Outline each Plasmodium falciparum-infected red blood cell.
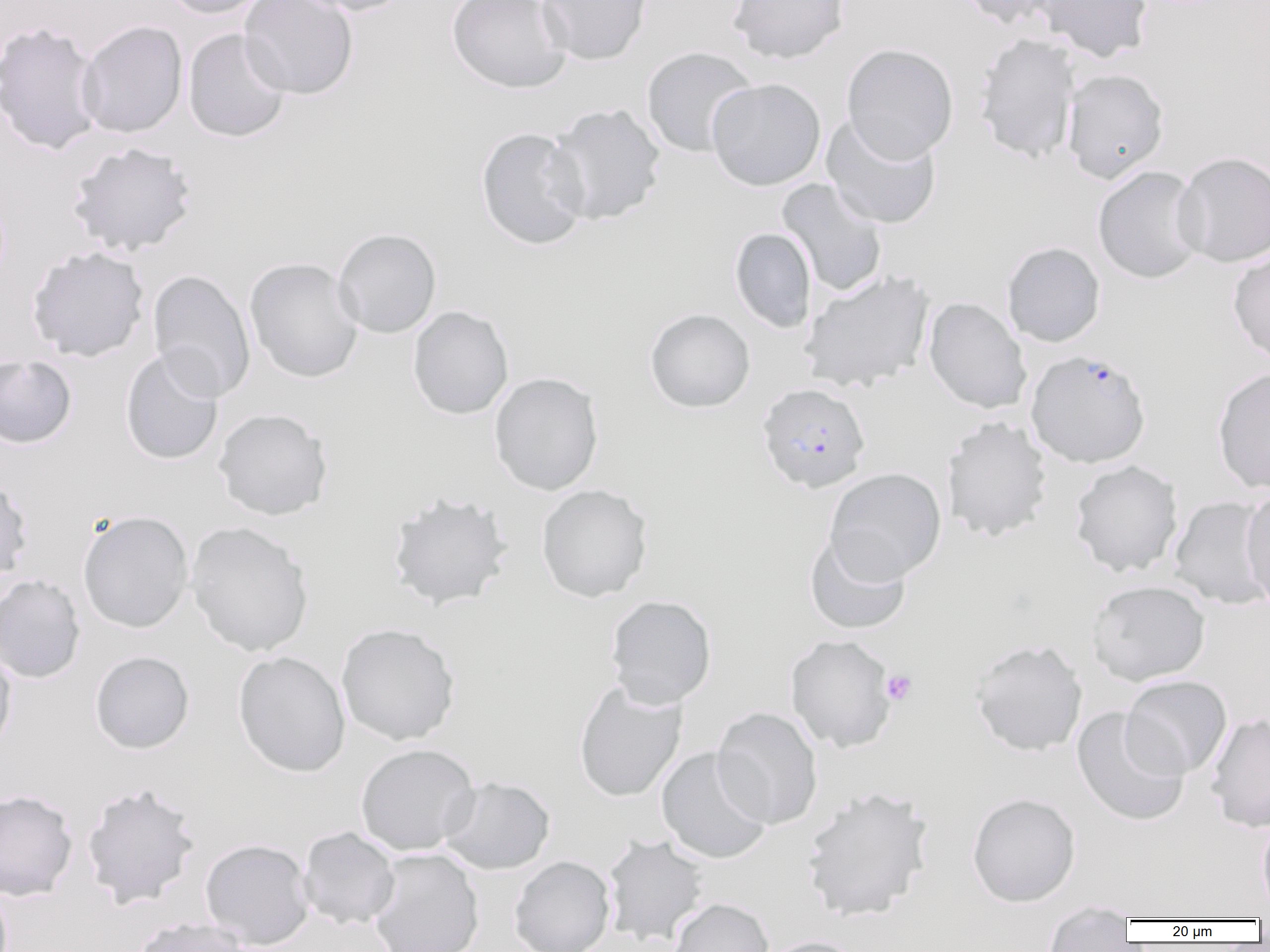
Approximate bounding boxes as named x1/y1/x2/y2 corners in pixels.
Plasmodium falciparum-infected red blood cells: (x1=1026, y1=348, x2=1151, y2=468), (x1=756, y1=382, x2=871, y2=493).

Uninfected red blood cell locations: (x1=160, y1=0, x2=271, y2=19), (x1=239, y1=0, x2=358, y2=99), (x1=295, y1=0, x2=415, y2=16), (x1=447, y1=0, x2=571, y2=94), (x1=536, y1=0, x2=652, y2=65), (x1=728, y1=0, x2=849, y2=64), (x1=955, y1=0, x2=1066, y2=28), (x1=1035, y1=0, x2=1154, y2=62), (x1=0, y1=21, x2=105, y2=157), (x1=77, y1=21, x2=188, y2=138), (x1=183, y1=28, x2=291, y2=142), (x1=974, y1=33, x2=1080, y2=163), (x1=842, y1=43, x2=959, y2=162), (x1=641, y1=46, x2=758, y2=157), (x1=1062, y1=68, x2=1170, y2=183), (x1=706, y1=78, x2=826, y2=191), (x1=547, y1=103, x2=666, y2=225), (x1=821, y1=115, x2=942, y2=230), (x1=475, y1=127, x2=591, y2=250), (x1=67, y1=141, x2=197, y2=258), (x1=1173, y1=151, x2=1270, y2=267), (x1=1093, y1=166, x2=1207, y2=284), (x1=777, y1=178, x2=888, y2=297), (x1=729, y1=227, x2=817, y2=333), (x1=333, y1=228, x2=442, y2=338), (x1=1002, y1=241, x2=1106, y2=347), (x1=27, y1=246, x2=149, y2=362), (x1=1228, y1=247, x2=1270, y2=366), (x1=244, y1=257, x2=364, y2=383), (x1=147, y1=269, x2=256, y2=402), (x1=799, y1=269, x2=935, y2=393), (x1=924, y1=297, x2=1032, y2=414), (x1=407, y1=306, x2=513, y2=420), (x1=644, y1=308, x2=755, y2=413), (x1=120, y1=348, x2=225, y2=465), (x1=0, y1=354, x2=77, y2=449), (x1=1212, y1=367, x2=1270, y2=494), (x1=489, y1=372, x2=604, y2=495), (x1=213, y1=407, x2=333, y2=520), (x1=941, y1=416, x2=1053, y2=542), (x1=1069, y1=460, x2=1183, y2=577), (x1=824, y1=467, x2=946, y2=585), (x1=0, y1=473, x2=33, y2=590), (x1=536, y1=484, x2=653, y2=603), (x1=1240, y1=485, x2=1270, y2=614), (x1=386, y1=491, x2=513, y2=611), (x1=1169, y1=495, x2=1270, y2=609), (x1=77, y1=510, x2=194, y2=633), (x1=185, y1=521, x2=314, y2=658), (x1=804, y1=531, x2=912, y2=635), (x1=0, y1=573, x2=86, y2=684), (x1=1087, y1=580, x2=1210, y2=686), (x1=605, y1=594, x2=717, y2=709), (x1=336, y1=622, x2=461, y2=746), (x1=785, y1=634, x2=897, y2=753), (x1=969, y1=639, x2=1088, y2=756), (x1=0, y1=646, x2=17, y2=757), (x1=89, y1=650, x2=194, y2=754), (x1=232, y1=650, x2=351, y2=777), (x1=1121, y1=674, x2=1233, y2=779), (x1=573, y1=681, x2=687, y2=802), (x1=712, y1=706, x2=823, y2=830), (x1=1071, y1=706, x2=1190, y2=827), (x1=1206, y1=713, x2=1270, y2=832), (x1=355, y1=743, x2=481, y2=856), (x1=656, y1=747, x2=774, y2=864), (x1=438, y1=776, x2=555, y2=875), (x1=80, y1=782, x2=201, y2=908), (x1=801, y1=785, x2=934, y2=923), (x1=0, y1=789, x2=78, y2=901), (x1=967, y1=792, x2=1081, y2=906), (x1=1257, y1=817, x2=1270, y2=916), (x1=298, y1=826, x2=401, y2=930), (x1=602, y1=834, x2=710, y2=946), (x1=199, y1=838, x2=315, y2=949), (x1=367, y1=848, x2=485, y2=952), (x1=509, y1=855, x2=615, y2=952), (x1=668, y1=897, x2=774, y2=952), (x1=1042, y1=904, x2=1137, y2=951), (x1=131, y1=917, x2=250, y2=952), (x1=758, y1=936, x2=867, y2=952). Platelet locations: (x1=881, y1=669, x2=918, y2=706). Slide-level diagnosis: Plasmodium falciparum. 1000x magnification. Single field of view. Image is 1270×952 pixels. Thin blood film. Light microscopy.